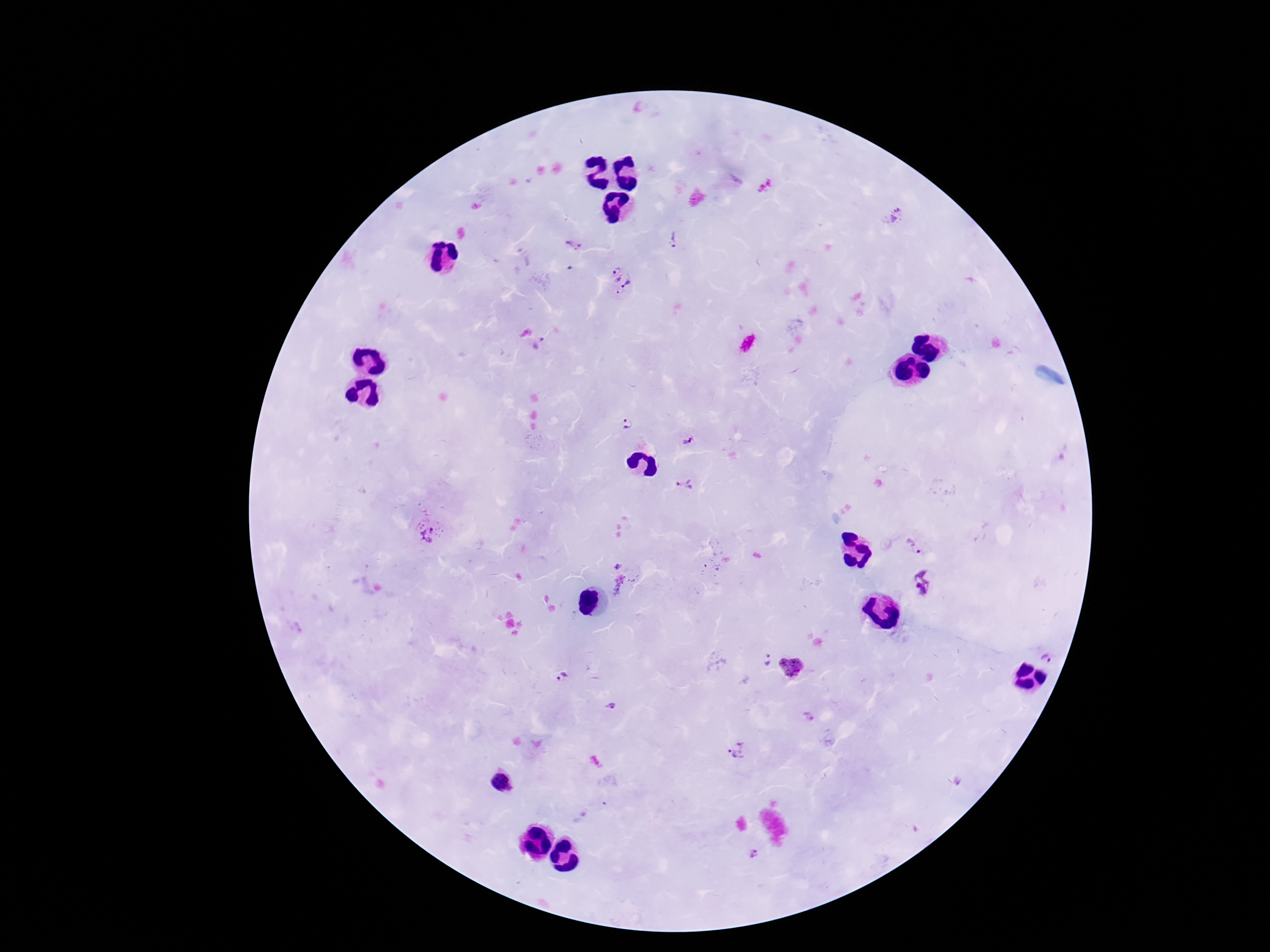
Approximate object centers, in pixels from the top-left corner.
Summary:
  - Plasmodium parasite locations: (x=896, y=215), (x=673, y=240), (x=575, y=246), (x=620, y=281), (x=540, y=344), (x=627, y=425), (x=688, y=440), (x=684, y=484), (x=429, y=536), (x=914, y=546), (x=618, y=566), (x=924, y=583), (x=1049, y=657), (x=767, y=660), (x=790, y=668), (x=563, y=677), (x=611, y=709), (x=809, y=718), (x=738, y=751), (x=756, y=855)
  - Preparation: thick peripheral-blood smear
  - Field of view: single
  - Stain: Giemsa
  - Image size: 1270×952 pixels
  - Magnification: 100x
  - Patient malaria status: positive
  - Capture: smartphone camera through the microscope eyepiece